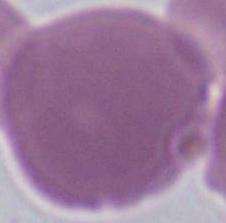 A red blood cell is seen. Photomicrograph. Captured at 1000x magnification.